Locate every leukocyte (white blood cell).
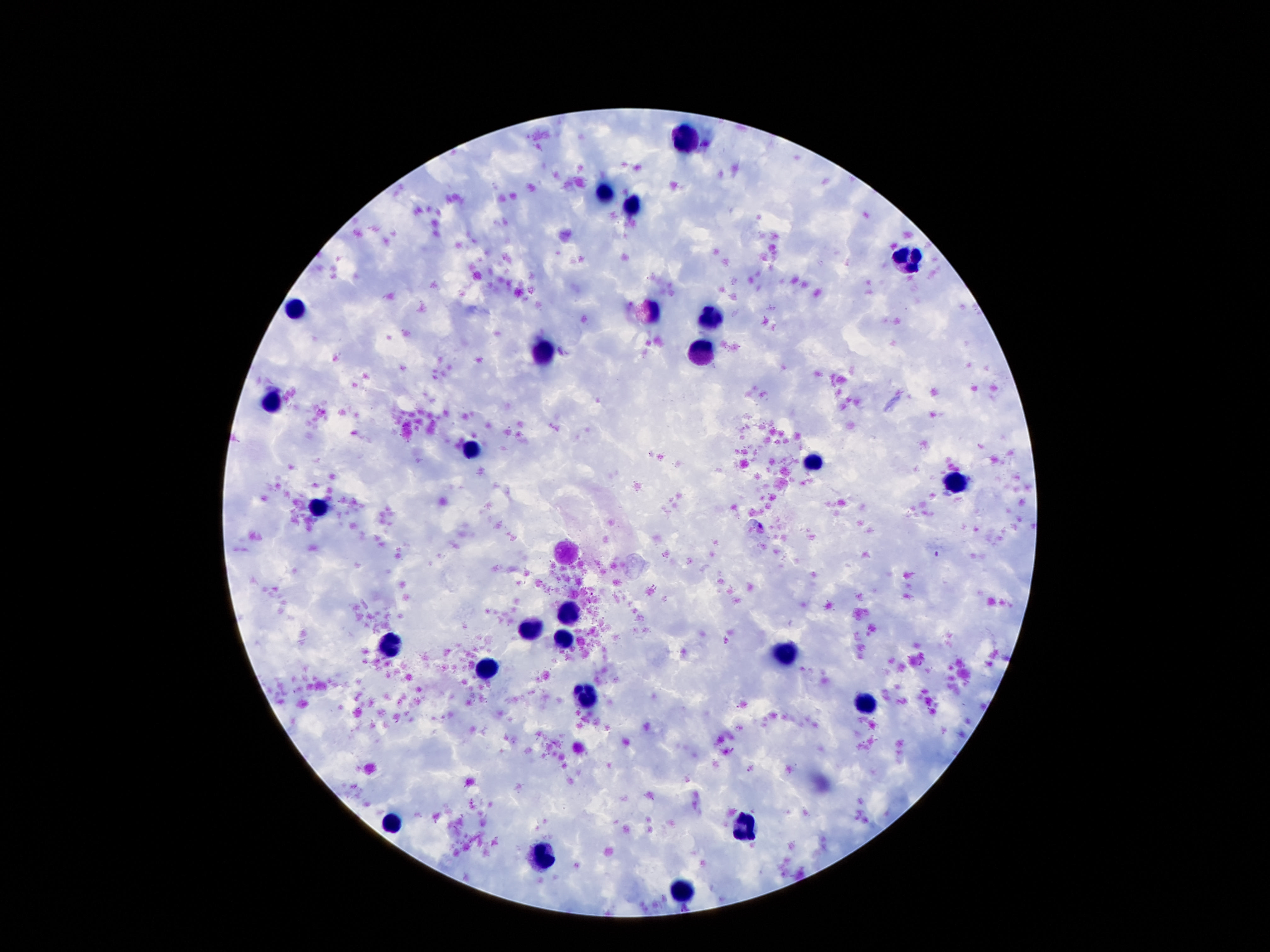
Approximate centers as [x, y] in pixels.
Leukocytes: [686, 139], [603, 194], [634, 207], [907, 261], [296, 309], [651, 311], [712, 319], [703, 345], [542, 347], [271, 405], [472, 450], [815, 465], [957, 481], [319, 508], [571, 610], [533, 628], [567, 639], [393, 648], [791, 655], [487, 666], [584, 694], [865, 704], [390, 821], [745, 824], [544, 857], [680, 889].

Patient malaria status: uninfected. Thick blood film. Single field of view. Image is 1270×952 pixels. 100x magnification. Giemsa stain. Photographed through the microscope eyepiece with a smartphone camera.